Report the malaria status of this cell.
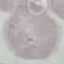

Uninfected.

preparation = thin blood smear
image type = automatically extracted cell patch, resized to 64 × 64 pixels
capture = smartphone through the microscope eyepiece
stain = Giemsa